Give the position of every malaria parasite.
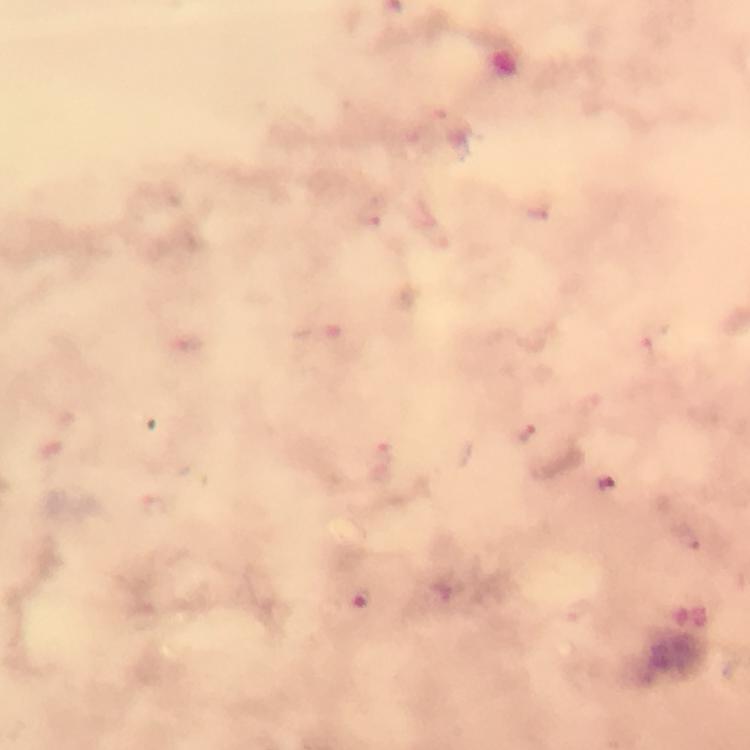
Approximate object centers, in pixels from the top-left corner.
Malaria parasites: (x=373, y=211), (x=650, y=351), (x=527, y=435), (x=686, y=536), (x=359, y=599).

From a diagnostic examination for malaria. Photographed through the microscope with a smartphone camera. Immersion oil applied. Thick blood smear. Giemsa stain. A crop from one field of view. Image is 750×750 pixels. 100x magnification.